Look for parasitized red blood cells.
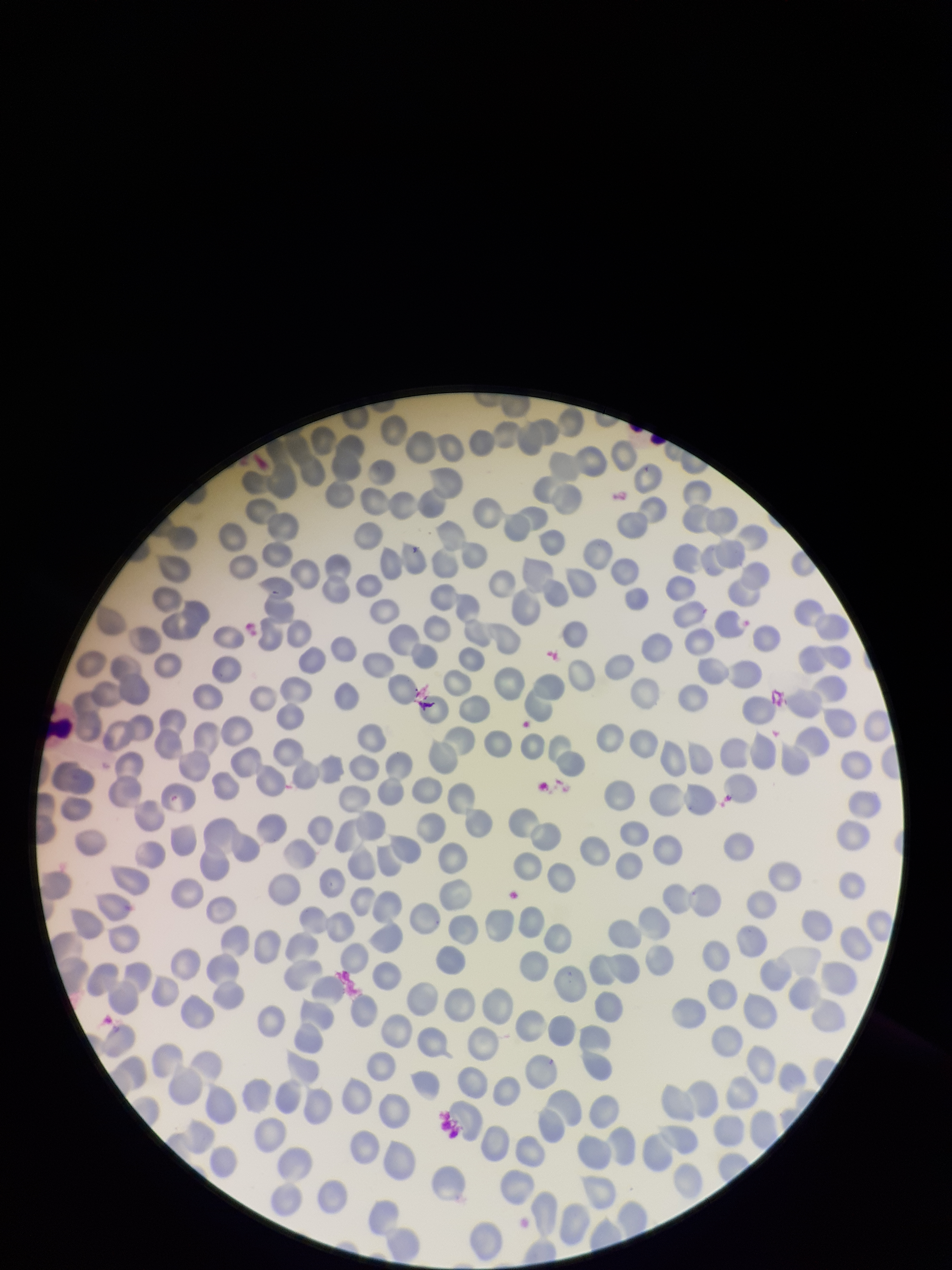
None seen.

Stained with Giemsa. Single field of view. Patient malaria status: negative. Preparation: thin. Parasitized red blood cell count: 0. Smartphone photograph taken through the eyepiece of a microscope. Red blood cell count: 312. Image is 952×1270 pixels.